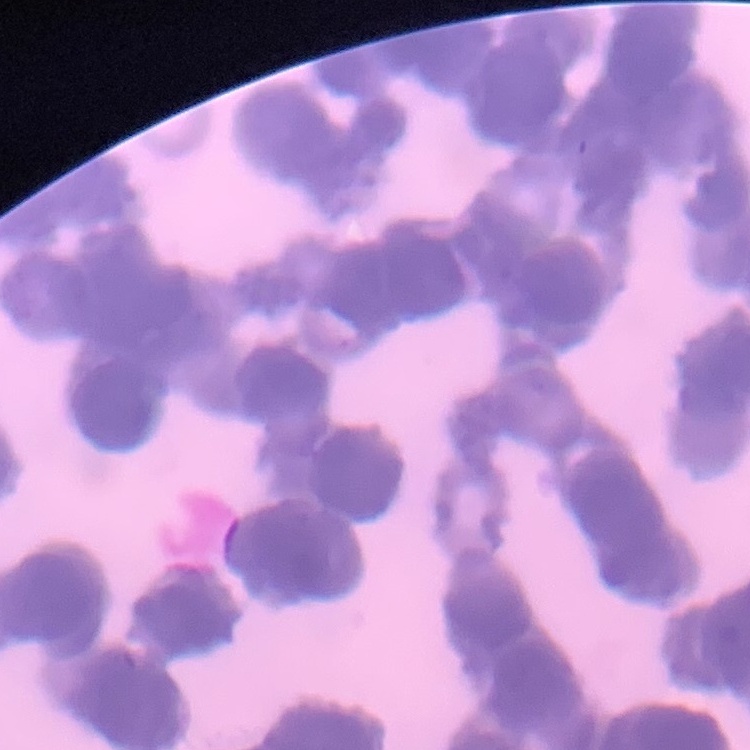
The erythrocytes show rouleaux formation. Square crop of a larger photomicrograph. Thin blood film. Field's or Giemsa stain.